Outline each blood parasite and name the species.
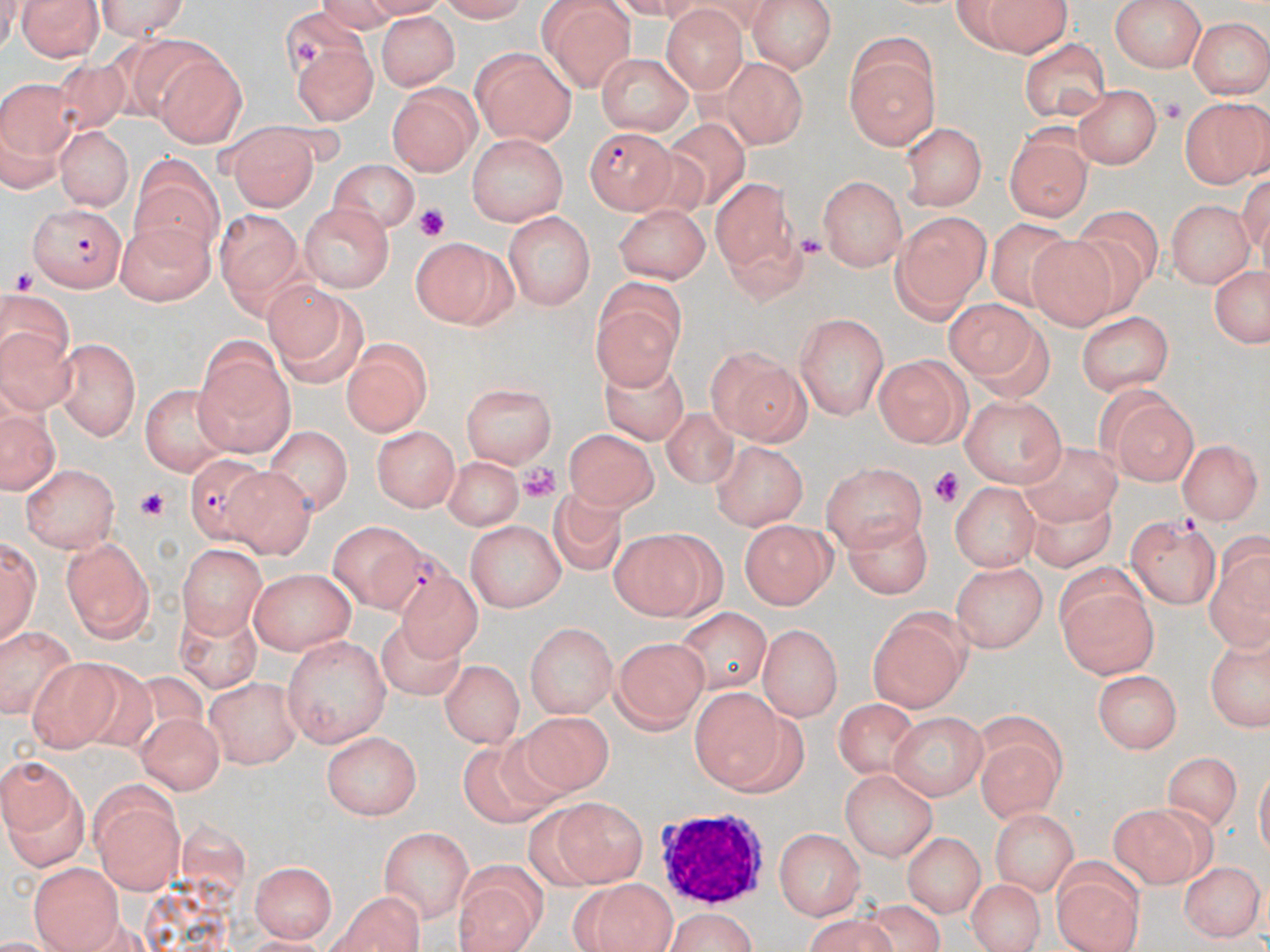

Approximate bounding boxes as named x1/y1/x2/y2 corners in pixels.
Plasmodium falciparum-infected red blood cells: (x1=585, y1=127, x2=674, y2=214), (x1=28, y1=201, x2=126, y2=290), (x1=180, y1=454, x2=276, y2=543), (x1=368, y1=545, x2=459, y2=625).
No Plasmodium ovale, Plasmodium malariae, Plasmodium vivax, Babesia divergens, or Trypanosoma brucei observed.

Uninfected red blood cell locations: (x1=16, y1=0, x2=105, y2=62), (x1=90, y1=0, x2=197, y2=40), (x1=430, y1=0, x2=535, y2=23), (x1=747, y1=0, x2=840, y2=74), (x1=951, y1=1, x2=1077, y2=56), (x1=539, y1=2, x2=634, y2=90), (x1=1113, y1=2, x2=1204, y2=73), (x1=273, y1=4, x2=368, y2=85), (x1=660, y1=5, x2=749, y2=92), (x1=373, y1=12, x2=459, y2=91), (x1=1189, y1=16, x2=1267, y2=98), (x1=106, y1=37, x2=215, y2=117), (x1=1021, y1=39, x2=1111, y2=121), (x1=291, y1=40, x2=378, y2=122), (x1=843, y1=41, x2=941, y2=148), (x1=473, y1=46, x2=577, y2=146), (x1=595, y1=51, x2=695, y2=133), (x1=48, y1=54, x2=137, y2=130), (x1=156, y1=54, x2=245, y2=142), (x1=717, y1=59, x2=809, y2=145), (x1=0, y1=77, x2=84, y2=171), (x1=1074, y1=83, x2=1162, y2=169), (x1=391, y1=84, x2=480, y2=173), (x1=1181, y1=96, x2=1270, y2=187), (x1=666, y1=113, x2=762, y2=206), (x1=901, y1=120, x2=986, y2=210), (x1=1003, y1=124, x2=1093, y2=222), (x1=54, y1=125, x2=134, y2=209), (x1=224, y1=129, x2=316, y2=209), (x1=465, y1=133, x2=567, y2=226), (x1=609, y1=139, x2=703, y2=238), (x1=331, y1=159, x2=419, y2=233), (x1=817, y1=174, x2=906, y2=271), (x1=712, y1=178, x2=787, y2=271), (x1=131, y1=182, x2=220, y2=268), (x1=1165, y1=198, x2=1252, y2=287), (x1=612, y1=200, x2=711, y2=284), (x1=297, y1=203, x2=395, y2=295), (x1=1078, y1=203, x2=1162, y2=291), (x1=209, y1=209, x2=302, y2=293), (x1=503, y1=210, x2=593, y2=309), (x1=891, y1=210, x2=992, y2=320), (x1=113, y1=217, x2=216, y2=305), (x1=985, y1=218, x2=1079, y2=312), (x1=1026, y1=234, x2=1114, y2=339), (x1=413, y1=236, x2=517, y2=327), (x1=1204, y1=263, x2=1270, y2=353), (x1=591, y1=278, x2=686, y2=388), (x1=264, y1=282, x2=367, y2=389), (x1=3, y1=289, x2=78, y2=411), (x1=944, y1=299, x2=1036, y2=387), (x1=1077, y1=309, x2=1174, y2=397), (x1=796, y1=311, x2=889, y2=419), (x1=55, y1=336, x2=143, y2=440), (x1=342, y1=341, x2=430, y2=437), (x1=191, y1=344, x2=296, y2=455), (x1=705, y1=347, x2=811, y2=446), (x1=873, y1=355, x2=969, y2=447), (x1=595, y1=358, x2=690, y2=447), (x1=137, y1=380, x2=234, y2=474), (x1=460, y1=383, x2=557, y2=467), (x1=1092, y1=384, x2=1198, y2=485), (x1=959, y1=396, x2=1067, y2=488), (x1=1, y1=406, x2=58, y2=494), (x1=662, y1=408, x2=743, y2=488), (x1=374, y1=424, x2=463, y2=510), (x1=260, y1=425, x2=348, y2=509), (x1=565, y1=426, x2=656, y2=508), (x1=710, y1=439, x2=805, y2=530), (x1=1181, y1=439, x2=1259, y2=526), (x1=1018, y1=442, x2=1128, y2=526), (x1=439, y1=453, x2=527, y2=530), (x1=821, y1=459, x2=927, y2=550), (x1=20, y1=463, x2=121, y2=552), (x1=231, y1=467, x2=319, y2=563), (x1=949, y1=480, x2=1038, y2=572), (x1=550, y1=489, x2=623, y2=581), (x1=1022, y1=495, x2=1119, y2=569), (x1=1126, y1=514, x2=1221, y2=607), (x1=843, y1=516, x2=935, y2=597), (x1=740, y1=517, x2=838, y2=609), (x1=464, y1=519, x2=563, y2=613), (x1=326, y1=520, x2=415, y2=612), (x1=610, y1=528, x2=719, y2=618), (x1=1, y1=534, x2=41, y2=650), (x1=60, y1=539, x2=155, y2=643), (x1=175, y1=543, x2=260, y2=639), (x1=1201, y1=546, x2=1270, y2=652), (x1=954, y1=558, x2=1049, y2=652), (x1=249, y1=569, x2=356, y2=653), (x1=1057, y1=577, x2=1158, y2=679), (x1=401, y1=585, x2=489, y2=665), (x1=867, y1=604, x2=972, y2=712), (x1=675, y1=608, x2=773, y2=689), (x1=172, y1=609, x2=265, y2=692), (x1=525, y1=620, x2=617, y2=718), (x1=2, y1=623, x2=75, y2=725), (x1=758, y1=623, x2=843, y2=720), (x1=377, y1=626, x2=467, y2=705), (x1=1203, y1=631, x2=1270, y2=733), (x1=610, y1=632, x2=708, y2=733), (x1=281, y1=634, x2=392, y2=748), (x1=110, y1=656, x2=206, y2=751), (x1=440, y1=657, x2=523, y2=750), (x1=28, y1=659, x2=121, y2=750), (x1=1093, y1=670, x2=1182, y2=753), (x1=206, y1=673, x2=301, y2=765), (x1=692, y1=685, x2=780, y2=791), (x1=831, y1=693, x2=922, y2=778), (x1=886, y1=711, x2=987, y2=799), (x1=137, y1=712, x2=222, y2=792), (x1=524, y1=714, x2=616, y2=794), (x1=324, y1=730, x2=422, y2=820), (x1=970, y1=737, x2=1061, y2=824), (x1=451, y1=741, x2=552, y2=824), (x1=1157, y1=751, x2=1241, y2=834), (x1=0, y1=756, x2=89, y2=874), (x1=838, y1=766, x2=942, y2=860), (x1=89, y1=783, x2=186, y2=894), (x1=557, y1=797, x2=647, y2=885), (x1=1111, y1=802, x2=1212, y2=880), (x1=996, y1=807, x2=1079, y2=887), (x1=772, y1=824, x2=863, y2=919), (x1=377, y1=827, x2=470, y2=920), (x1=901, y1=831, x2=984, y2=917), (x1=252, y1=856, x2=335, y2=944), (x1=1183, y1=859, x2=1261, y2=940), (x1=29, y1=862, x2=122, y2=951), (x1=456, y1=862, x2=546, y2=949), (x1=1047, y1=873, x2=1148, y2=952), (x1=965, y1=875, x2=1044, y2=952), (x1=576, y1=878, x2=676, y2=952), (x1=330, y1=885, x2=429, y2=952), (x1=663, y1=909, x2=759, y2=952), (x1=800, y1=916, x2=898, y2=951). White blood cell locations: (x1=656, y1=806, x2=776, y2=903). Platelet locations: (x1=292, y1=39, x2=320, y2=64), (x1=1155, y1=93, x2=1192, y2=131), (x1=414, y1=203, x2=451, y2=244), (x1=790, y1=229, x2=829, y2=264), (x1=7, y1=265, x2=46, y2=301), (x1=516, y1=460, x2=560, y2=504), (x1=930, y1=468, x2=965, y2=506), (x1=135, y1=486, x2=169, y2=523). Slide-level diagnosis: Plasmodium falciparum. May-Grünwald-Giemsa-stained preparation. One field of a larger specimen. Thin blood smear. Optical microscopy. Image is 1270×952 pixels. Captured at 1000x magnification.